Report the malaria status of this cell.
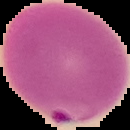

It is parasitized.

Segmented cell region on a black background. Image is 130×130 pixels. From a thin blood smear.